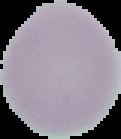

result = no Plasmodium parasites detected
preparation = thin blood smear
image size = 121×139 pixels
image type = segmented cell region with the area outside set to black